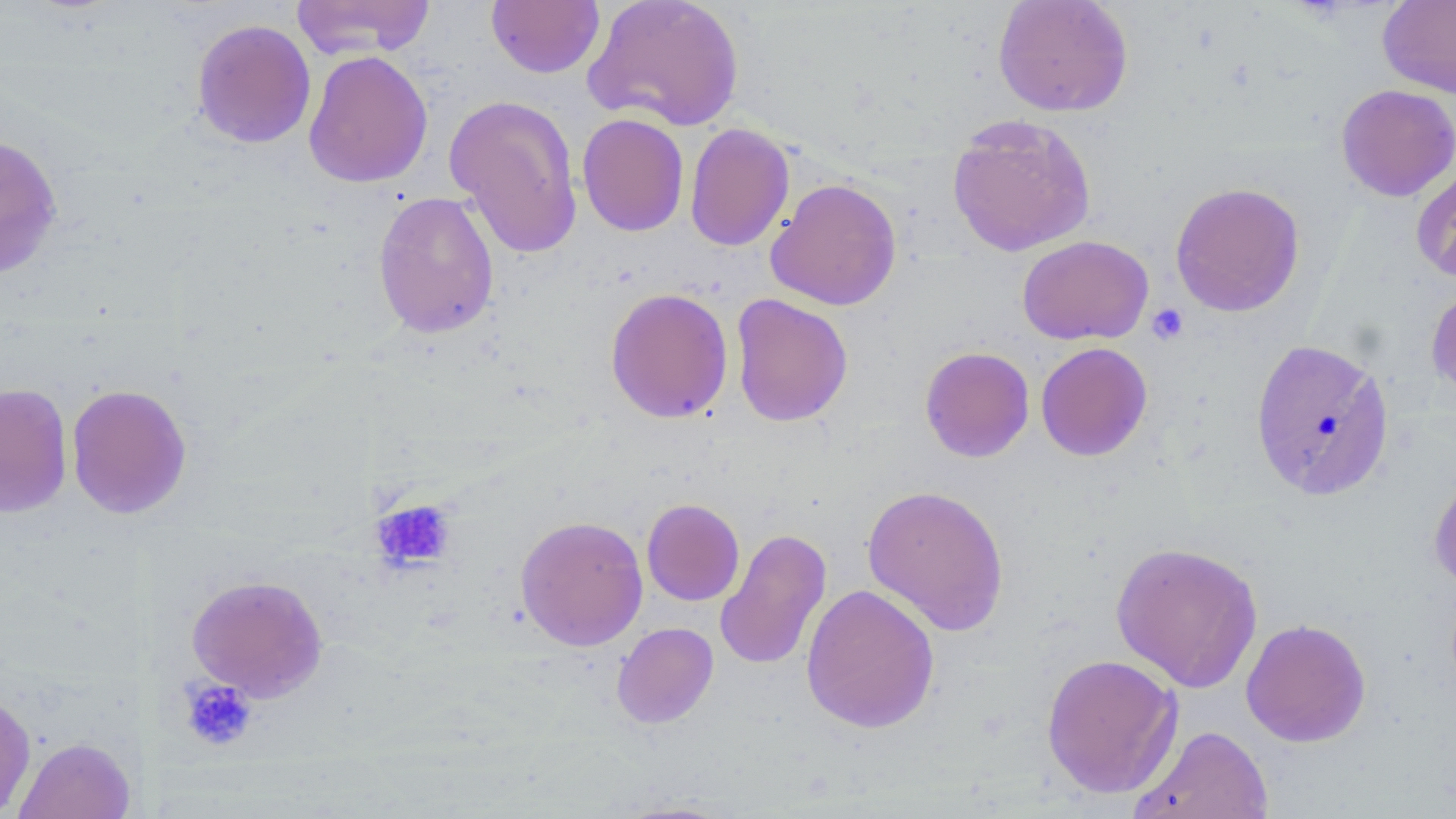

slide-level diagnosis = negative for blood parasites
stain = May-Grünwald-Giemsa
image size = 1456×819 pixels
magnification = 1000x
uninfected red blood cell locations = approximate bounding boxes as [x1, y1, x2, y2] in pixels: [290, 0, 436, 59], [582, 0, 745, 132], [992, 0, 1133, 117], [1377, 0, 1456, 99], [485, 1, 605, 78], [191, 18, 316, 148], [303, 50, 433, 188], [1335, 84, 1456, 201], [444, 93, 583, 259], [576, 113, 689, 237], [946, 114, 1096, 258], [684, 123, 794, 251], [0, 133, 64, 279], [1411, 159, 1456, 287], [765, 178, 903, 311], [1169, 182, 1306, 318], [372, 191, 500, 339], [1016, 235, 1154, 346], [1426, 283, 1456, 405], [605, 287, 733, 423], [730, 293, 853, 427], [1249, 337, 1396, 502], [1035, 342, 1153, 461], [920, 345, 1035, 462], [0, 382, 73, 518], [66, 383, 192, 519], [1428, 465, 1456, 593], [860, 483, 1010, 636], [641, 498, 745, 605], [514, 514, 648, 651], [715, 527, 832, 671], [1110, 541, 1264, 693], [186, 573, 329, 702], [800, 583, 940, 734], [1241, 618, 1371, 747], [611, 622, 718, 728], [1040, 653, 1184, 799], [0, 690, 36, 817], [1129, 724, 1273, 818], [14, 736, 135, 819], [608, 798, 742, 818]
field of view = single
platelet locations = approximate bounding boxes as [x1, y1, x2, y2] in pixels: [1147, 304, 1188, 344], [371, 498, 456, 571], [178, 678, 258, 751]
modality = optical microscopy
preparation = thin blood film